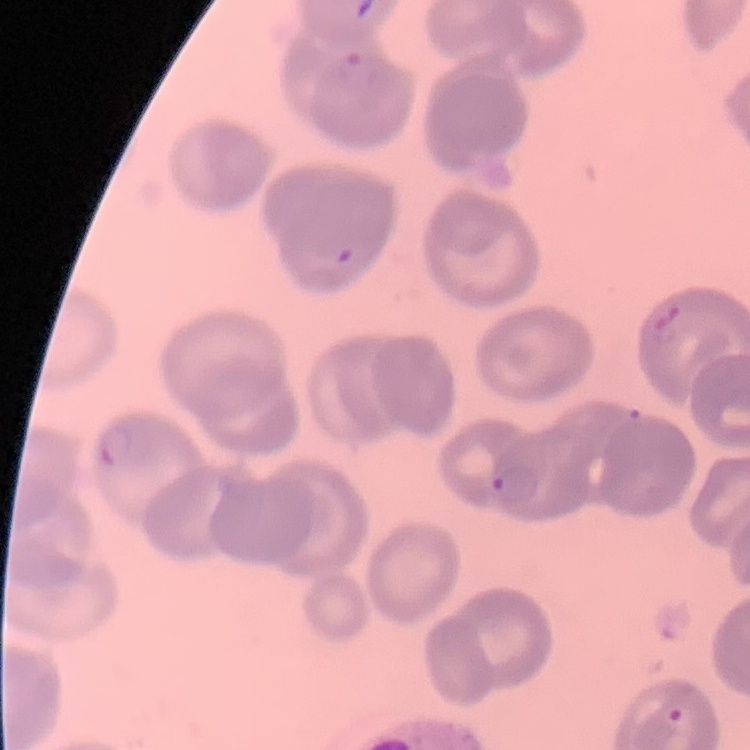
erythrocyte_morphology: no rouleaux formation
stain: Field's or Giemsa
image_type: square crop of a larger photomicrograph
preparation: thin peripheral smear